Identify the cell.
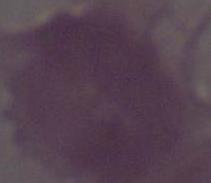
An erythrocyte.

1000x magnification. Micrograph.